Point out each malaria parasite.
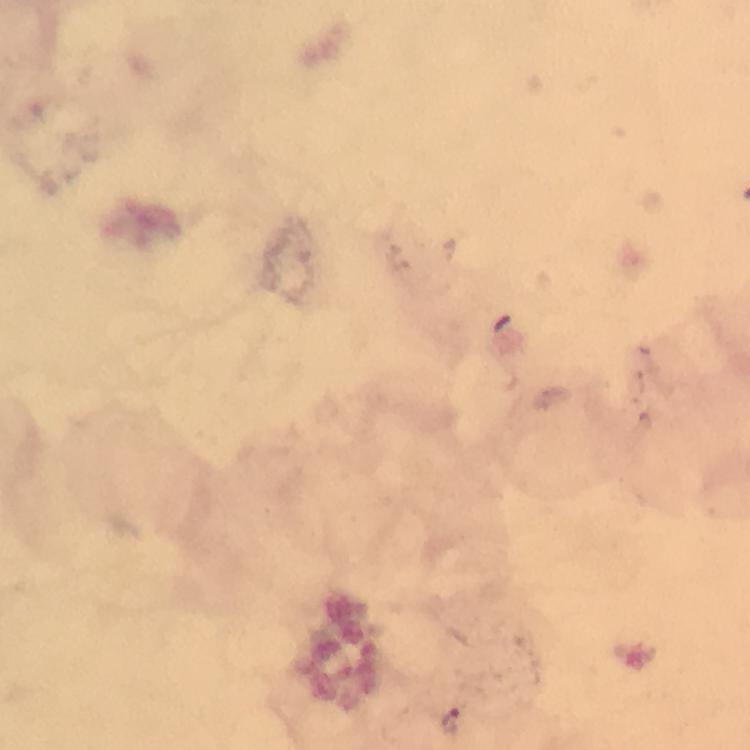

Approximate centers as (x, y) in pixels.
Malaria parasites: (452, 722).

capture: smartphone photograph through a microscope
stain: Giemsa
preparation: thick smear
immersion_oil: used
image_size: 750×750 pixels
context: from a malaria diagnostic workup
cropped_from: a single field of view
magnification: 100x